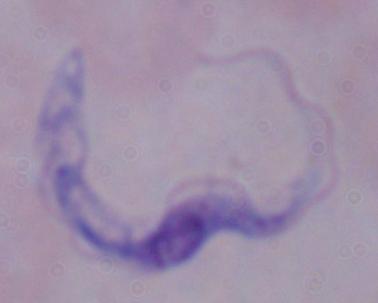 Photomicrograph. A trypanosome is shown. Captured at 1000x magnification.